Classify this cell by malaria status.
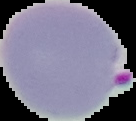
Parasitized.

Image is 136×121 pixels. Segmented cell region on a black background. From a thin blood smear.